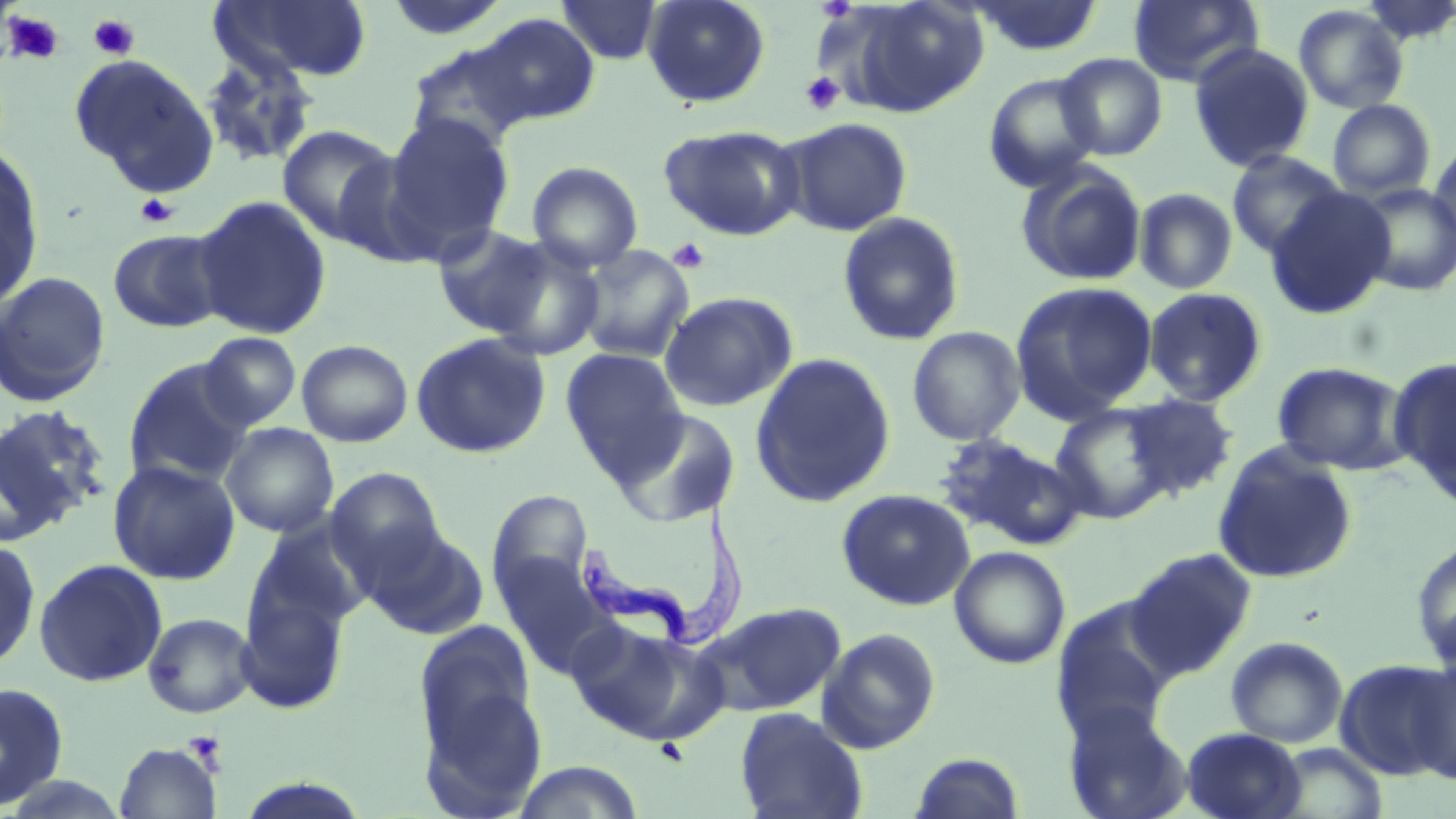

Approximate bounding boxes as (x1, y1, x2, y2) in pixels. Platelet locations: (3, 11, 66, 65), (88, 13, 140, 60), (800, 71, 845, 115), (135, 193, 179, 228), (667, 238, 711, 274), (182, 730, 228, 771). Uninfected red blood cell locations: (212, 0, 373, 84), (383, 0, 512, 41), (642, 0, 771, 108), (829, 0, 991, 118), (968, 0, 1105, 57), (1129, 0, 1263, 87), (556, 1, 663, 64), (1293, 4, 1409, 114), (473, 13, 601, 128), (404, 41, 535, 156), (1188, 42, 1315, 173), (198, 51, 320, 169), (1056, 52, 1167, 160), (69, 53, 219, 196), (983, 71, 1103, 192), (1327, 99, 1436, 199), (382, 113, 514, 256), (780, 116, 913, 237), (277, 124, 400, 247), (659, 124, 806, 241), (1428, 140, 1456, 249), (0, 148, 44, 311), (1226, 149, 1347, 258), (527, 161, 644, 272), (1015, 162, 1147, 287), (1352, 184, 1456, 297), (1134, 187, 1238, 295), (1265, 187, 1395, 320), (191, 195, 333, 341), (837, 211, 965, 346), (431, 224, 557, 340), (107, 228, 229, 333), (483, 238, 607, 360), (576, 245, 695, 363), (0, 270, 112, 408), (1010, 280, 1158, 421), (1143, 287, 1268, 406), (659, 291, 798, 412), (906, 325, 1026, 445), (410, 331, 551, 459), (197, 332, 302, 431), (297, 339, 413, 447), (560, 348, 688, 479), (749, 351, 896, 509), (1389, 357, 1456, 506), (123, 359, 255, 488), (1271, 362, 1410, 474), (1121, 392, 1239, 500), (1049, 402, 1177, 524), (0, 403, 110, 542), (612, 407, 742, 528), (220, 422, 339, 538), (934, 434, 1085, 550), (1212, 444, 1358, 585), (107, 458, 241, 585), (325, 468, 447, 582), (837, 488, 975, 610), (487, 489, 594, 602), (246, 521, 374, 640), (361, 524, 488, 640), (1411, 536, 1456, 671), (0, 538, 41, 671), (949, 546, 1070, 669), (1125, 546, 1258, 679), (493, 551, 611, 672), (33, 558, 167, 688), (236, 582, 351, 716), (1050, 601, 1174, 746), (693, 602, 846, 717), (142, 612, 257, 718), (414, 620, 538, 758), (567, 623, 723, 746), (817, 627, 942, 754), (1225, 636, 1349, 747), (1334, 658, 1455, 781), (1408, 658, 1456, 786), (418, 680, 548, 817), (0, 682, 69, 809), (1063, 703, 1192, 819), (734, 706, 869, 819), (1182, 727, 1306, 818), (114, 742, 221, 819), (1269, 742, 1389, 819), (908, 751, 1027, 818), (510, 760, 646, 819), (3, 773, 132, 817), (235, 778, 373, 818). Trypanosoma brucei locations: (579, 500, 752, 651). Slide-level diagnosis: Trypanosoma brucei. Thin blood film. Captured at 1000x magnification. Single field of view. May-Grünwald-Giemsa stain. Light microscopy. Image is 1456×819 pixels.